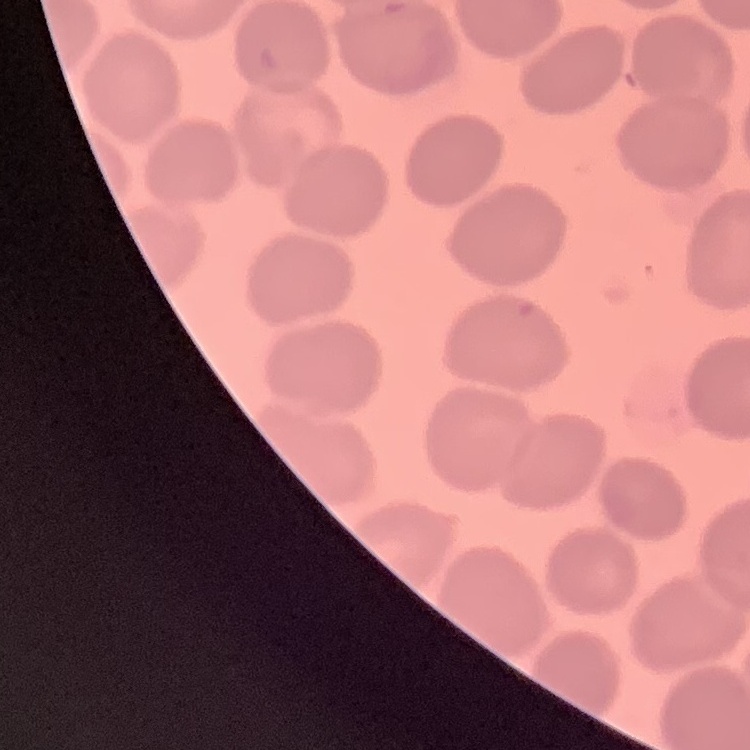

erythrocyte_morphology: no rouleaux formation
preparation: thin blood smear
image_type: one tile cut from a larger photomicrograph
stain: Field's or Giemsa